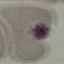
Result: negative for malaria parasites. Thin blood film. Photographed with a smartphone camera at the microscope eyepiece. Automatically extracted cell patch, resized to 64 × 64 pixels. Giemsa stain.